Report the malaria status of this cell.
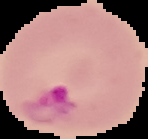

It is parasitized.

From a thin blood film. Segmented cell region on a black background. Image is 148×139 pixels.